Identify the blood parasite species.
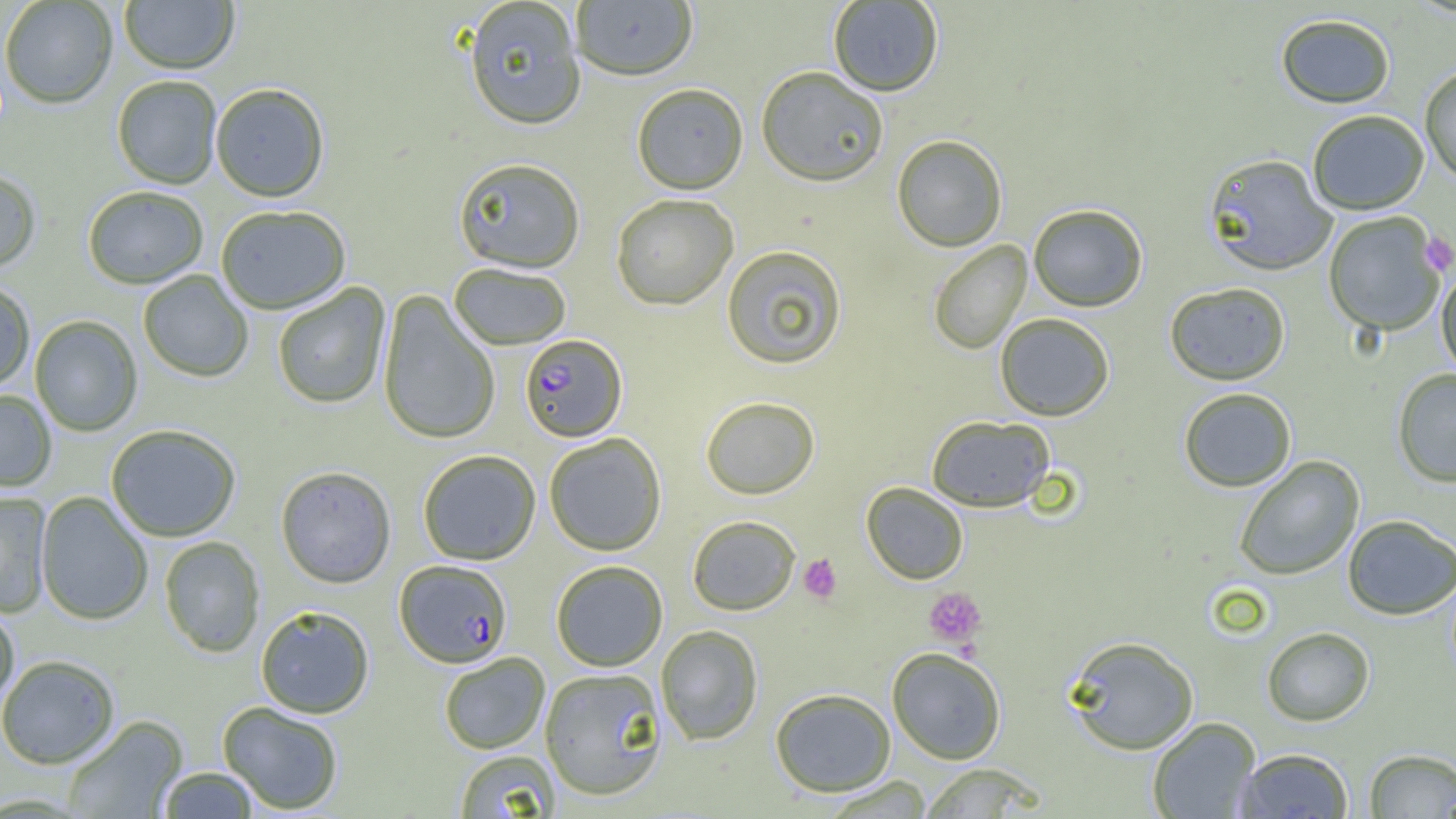

Plasmodium falciparum.

platelet locations = approximate bounding boxes as [x1, y1, x2, y2] in pixels: [1418, 232, 1456, 276], [798, 554, 841, 603], [924, 587, 987, 647]
field of view = single
preparation = thin blood film
image size = 1456×819 pixels
Plasmodium falciparum-infected red blood cell locations = approximate bounding boxes as [x1, y1, x2, y2] in pixels: [520, 334, 627, 443], [394, 560, 513, 668]
magnification = 1000x
modality = optical microscopy
uninfected red blood cell locations = approximate bounding boxes as [x1, y1, x2, y2] in pixels: [120, 0, 239, 76], [570, 0, 698, 83], [0, 1, 117, 110], [464, 1, 587, 132], [828, 1, 943, 97], [1275, 13, 1396, 109], [1419, 64, 1456, 185], [756, 68, 888, 187], [112, 77, 222, 190], [631, 84, 748, 196], [211, 85, 330, 203], [1306, 109, 1430, 215], [892, 134, 1007, 252], [1203, 152, 1338, 276], [453, 158, 586, 274], [0, 171, 40, 275], [83, 188, 208, 290], [611, 194, 738, 311], [1028, 204, 1148, 312], [216, 207, 351, 315], [1323, 212, 1446, 337], [928, 240, 1032, 354], [721, 245, 848, 370], [449, 264, 571, 350], [1436, 264, 1456, 381], [138, 271, 253, 383], [0, 281, 35, 392], [1164, 282, 1291, 386], [273, 283, 391, 410], [377, 291, 500, 446], [995, 313, 1115, 421], [29, 316, 143, 437], [1392, 368, 1456, 487], [1178, 387, 1297, 492], [0, 390, 56, 493], [700, 396, 820, 500], [926, 415, 1055, 512], [106, 425, 241, 543], [544, 433, 666, 556], [418, 451, 541, 565], [1233, 456, 1365, 581], [275, 466, 397, 589], [861, 482, 969, 584], [0, 492, 51, 619], [36, 492, 153, 626], [1342, 514, 1455, 620], [687, 515, 800, 616], [159, 537, 265, 658], [551, 560, 668, 671], [0, 606, 19, 715], [256, 607, 374, 719], [655, 624, 763, 745], [1261, 626, 1375, 726], [1063, 635, 1200, 755], [887, 647, 1006, 764], [439, 652, 550, 754], [0, 655, 120, 770], [539, 667, 668, 801], [770, 688, 896, 797], [217, 702, 344, 815], [62, 716, 188, 818], [1147, 717, 1262, 818], [1236, 747, 1353, 819], [1363, 748, 1456, 818], [454, 750, 561, 818], [918, 763, 1047, 817], [158, 767, 258, 818], [819, 775, 935, 818]